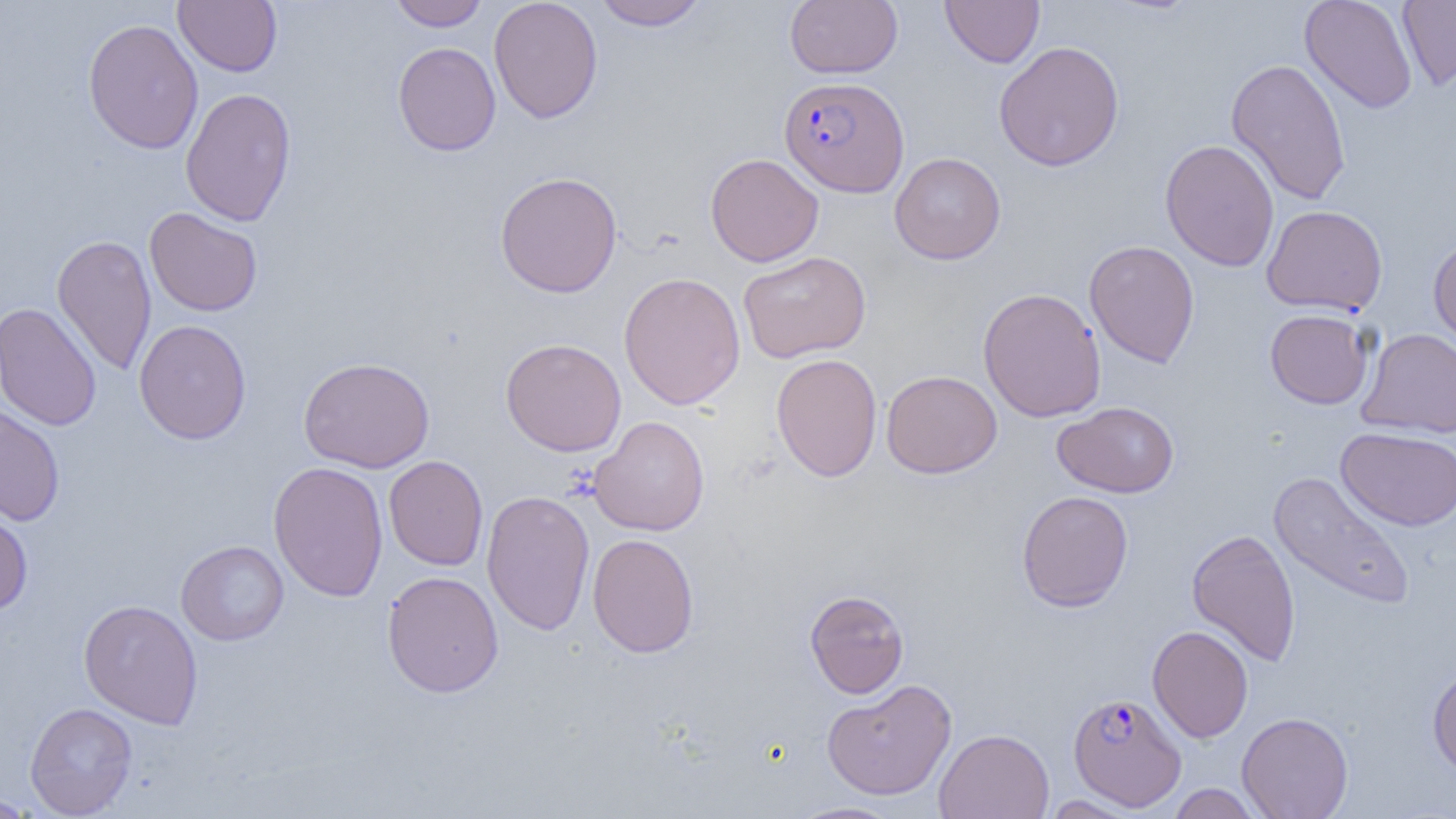

slide-level diagnosis = Plasmodium falciparum
magnification = 1000x
uninfected red blood cell locations = approximate bounding boxes as (x1,y1)-(x2,y2) corner pairs in pixels: (173,0)-(282,76), (390,0)-(489,30), (488,0)-(603,124), (592,0)-(707,30), (785,0)-(903,78), (940,0)-(1045,68), (1300,0)-(1417,113), (1397,0)-(1456,91), (82,18)-(203,154), (392,41)-(501,156), (993,41)-(1125,171), (1225,58)-(1352,205), (180,88)-(297,226), (1159,139)-(1279,272), (890,152)-(1006,264), (705,153)-(824,266), (494,171)-(623,298), (1262,205)-(1388,315), (144,207)-(263,317), (51,234)-(157,375), (1427,235)-(1456,355), (1084,240)-(1200,368), (738,251)-(871,363), (618,271)-(746,410), (978,287)-(1106,422), (0,302)-(102,432), (1265,308)-(1375,409), (134,319)-(251,444), (1357,327)-(1456,438), (500,337)-(626,457), (770,353)-(883,482), (298,356)-(435,473), (881,369)-(1003,478), (1052,401)-(1180,498), (0,404)-(65,527), (589,416)-(710,535), (1336,427)-(1456,531), (384,455)-(488,571), (267,461)-(389,602), (1268,470)-(1417,612), (481,490)-(596,635), (1017,490)-(1133,612), (0,505)-(33,615), (1187,528)-(1301,666), (587,533)-(699,658), (176,540)-(288,645), (382,570)-(504,698), (804,589)-(909,698), (78,599)-(204,729), (1147,625)-(1253,743), (1427,665)-(1456,777), (821,679)-(957,800), (25,702)-(138,818), (1237,711)-(1354,819), (934,728)-(1054,819), (1168,784)-(1265,818), (0,792)-(42,817), (1042,795)-(1143,818), (785,801)-(905,819)
preparation = thin blood smear
modality = light microscopy
field of view = one of a larger specimen
image size = 1456×819 pixels
Plasmodium falciparum-infected red blood cell locations = approximate bounding boxes as (x1,y1)-(x2,y2) corner pairs in pixels: (779,75)-(909,197), (1068,692)-(1187,811)